Name the blood parasite species.
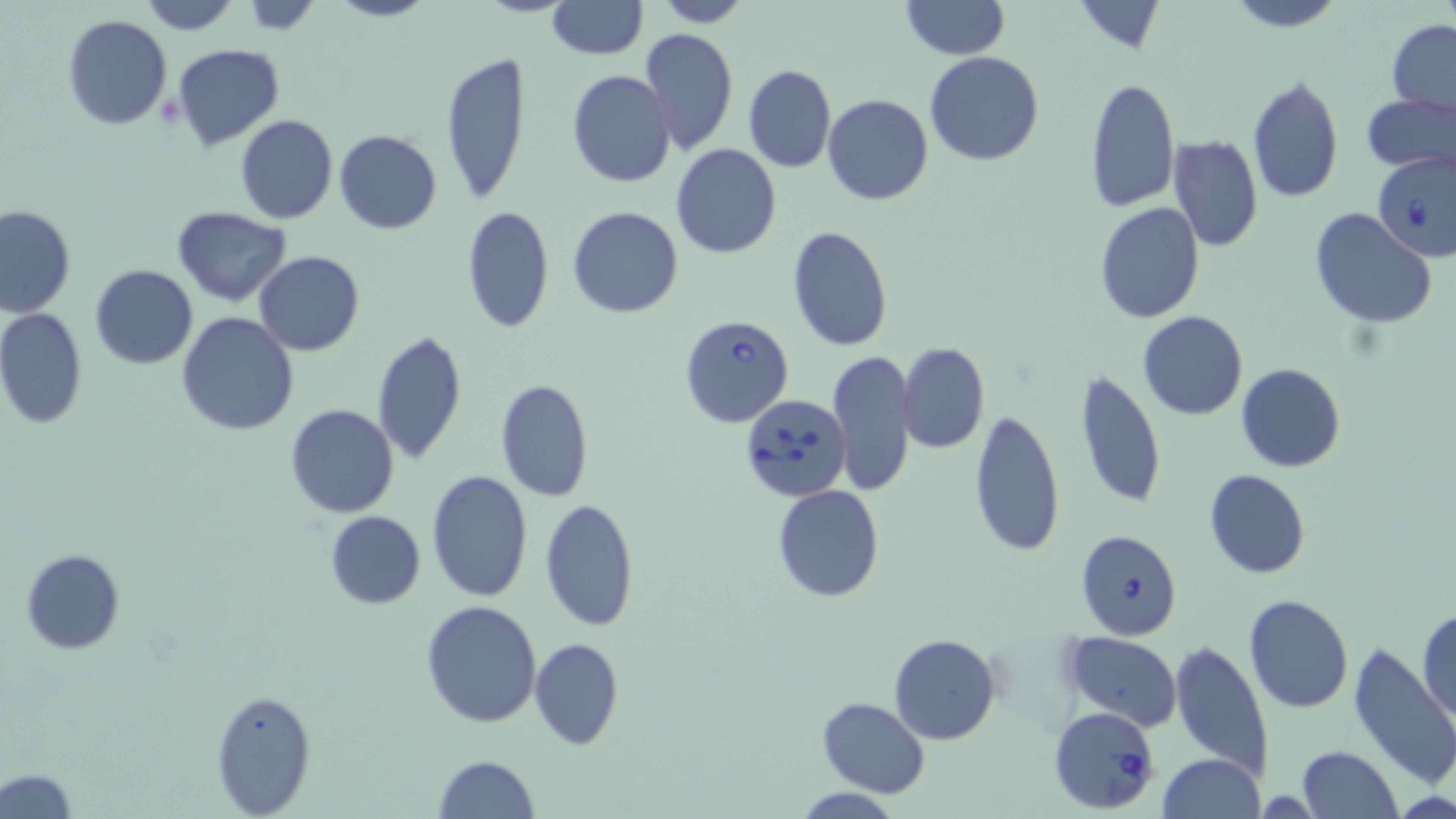
Babesia divergens.

Summary:
  - Coordinate format: approximate bounding boxes as (x1, y1, x2, y2) in pixels
  - Babesia divergens-infected red blood cell locations: (1371, 150, 1456, 262), (680, 316, 793, 428), (740, 394, 852, 502), (1076, 528, 1182, 641), (1047, 706, 1162, 815)
  - Uninfected red blood cell locations: (135, 0, 240, 35), (242, 0, 322, 33), (325, 0, 435, 22), (546, 0, 646, 59), (648, 0, 751, 27), (900, 0, 1008, 61), (1072, 0, 1166, 54), (1222, 0, 1347, 32), (61, 13, 174, 130), (1387, 20, 1456, 116), (638, 26, 737, 157), (171, 43, 285, 150), (925, 52, 1044, 167), (440, 53, 531, 205), (743, 64, 835, 173), (568, 70, 676, 188), (1246, 74, 1345, 204), (1085, 76, 1179, 213), (1361, 92, 1456, 178), (823, 93, 934, 205), (235, 115, 339, 224), (334, 129, 441, 235), (1167, 135, 1263, 251), (671, 144, 780, 259), (1094, 202, 1205, 323), (0, 205, 75, 318), (461, 206, 553, 333), (568, 206, 683, 317), (171, 207, 292, 306), (1309, 207, 1436, 328), (788, 225, 894, 352), (253, 250, 365, 355), (89, 264, 198, 370), (0, 308, 88, 429), (1137, 310, 1248, 422), (176, 312, 298, 435), (371, 329, 468, 468), (897, 342, 988, 453), (829, 350, 916, 497), (1236, 363, 1345, 473), (1074, 369, 1166, 512), (494, 378, 594, 503), (285, 405, 399, 518), (969, 409, 1064, 557), (1204, 469, 1310, 579), (427, 470, 532, 601), (772, 485, 885, 601), (539, 499, 639, 630), (324, 510, 426, 609), (21, 549, 124, 654), (1242, 593, 1354, 714), (421, 600, 543, 727), (1417, 609, 1456, 723), (1060, 633, 1183, 732), (888, 634, 1000, 744), (530, 637, 624, 750), (1170, 639, 1274, 779), (1347, 643, 1451, 791), (211, 689, 318, 818), (816, 697, 930, 798), (1297, 745, 1404, 819), (1156, 754, 1266, 818), (433, 755, 541, 818), (0, 768, 77, 817), (788, 788, 907, 818)
  - Preparation: thin blood film
  - Stain: May-Grünwald-Giemsa
  - Field of view: single
  - Image size: 1456×819 pixels
  - Modality: light microscopy
  - Magnification: 1000x